State the blood parasite species.
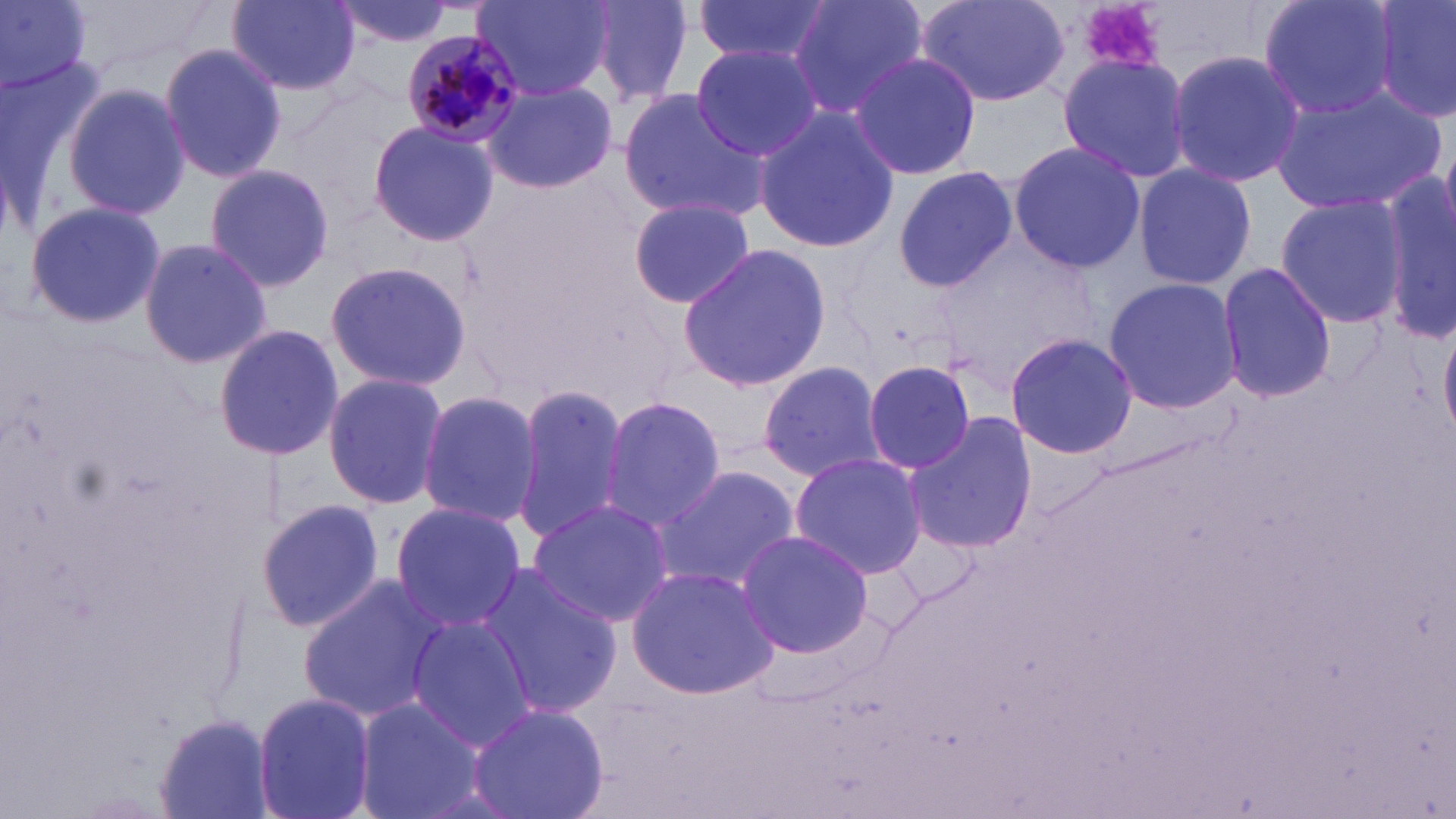
Plasmodium malariae.

Summary:
  - Coordinate format: approximate bounding boxes as named x1/y1/x2/y2 corners in pixels
  - Platelet locations: (x1=1073, y1=0, x2=1168, y2=75)
  - Uninfected red blood cell locations: (x1=0, y1=0, x2=91, y2=94), (x1=330, y1=0, x2=456, y2=48), (x1=473, y1=0, x2=612, y2=101), (x1=582, y1=0, x2=696, y2=105), (x1=691, y1=0, x2=837, y2=68), (x1=789, y1=0, x2=927, y2=119), (x1=917, y1=0, x2=1073, y2=106), (x1=1259, y1=0, x2=1400, y2=121), (x1=1373, y1=0, x2=1454, y2=126), (x1=227, y1=1, x2=362, y2=96), (x1=688, y1=43, x2=823, y2=162), (x1=158, y1=44, x2=287, y2=182), (x1=1163, y1=49, x2=1304, y2=185), (x1=849, y1=51, x2=983, y2=183), (x1=0, y1=55, x2=106, y2=217), (x1=1056, y1=55, x2=1191, y2=184), (x1=482, y1=80, x2=619, y2=195), (x1=62, y1=83, x2=192, y2=220), (x1=1270, y1=84, x2=1447, y2=212), (x1=618, y1=89, x2=770, y2=223), (x1=750, y1=105, x2=901, y2=255), (x1=366, y1=120, x2=499, y2=246), (x1=1008, y1=139, x2=1144, y2=274), (x1=204, y1=163, x2=334, y2=290), (x1=1131, y1=163, x2=1255, y2=289), (x1=1381, y1=164, x2=1456, y2=343), (x1=894, y1=168, x2=1018, y2=290), (x1=1274, y1=193, x2=1406, y2=325), (x1=628, y1=197, x2=756, y2=309), (x1=24, y1=201, x2=164, y2=328), (x1=139, y1=238, x2=271, y2=369), (x1=676, y1=243, x2=832, y2=392), (x1=321, y1=261, x2=473, y2=392), (x1=1217, y1=263, x2=1337, y2=402), (x1=1102, y1=276, x2=1242, y2=416), (x1=1440, y1=323, x2=1456, y2=441), (x1=215, y1=324, x2=344, y2=463), (x1=1004, y1=333, x2=1137, y2=460), (x1=755, y1=359, x2=887, y2=482), (x1=863, y1=359, x2=979, y2=475), (x1=321, y1=372, x2=447, y2=509), (x1=512, y1=384, x2=628, y2=543), (x1=417, y1=390, x2=544, y2=528), (x1=598, y1=395, x2=728, y2=530), (x1=903, y1=413, x2=1037, y2=555), (x1=789, y1=452, x2=927, y2=577), (x1=658, y1=464, x2=800, y2=593), (x1=525, y1=498, x2=673, y2=629), (x1=256, y1=500, x2=385, y2=632), (x1=390, y1=502, x2=524, y2=633), (x1=732, y1=529, x2=878, y2=659), (x1=475, y1=565, x2=623, y2=720), (x1=625, y1=565, x2=782, y2=700), (x1=296, y1=575, x2=445, y2=721), (x1=406, y1=615, x2=538, y2=748), (x1=252, y1=690, x2=377, y2=819), (x1=353, y1=700, x2=487, y2=819), (x1=467, y1=703, x2=608, y2=819), (x1=154, y1=714, x2=275, y2=819)
  - Plasmodium malariae-infected red blood cell locations: (x1=400, y1=30, x2=529, y2=148)
  - Modality: optical microscopy
  - Field of view: one of a larger specimen
  - Preparation: thin blood smear
  - Stain: May-Grünwald-Giemsa
  - Magnification: 1000x
  - Image size: 1456×819 pixels